Classify this cell by malaria status.
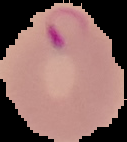
Parasitized.

image type = segmented cell region on a black background
image size = 127×142 pixels
preparation = thin blood film